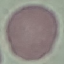 Malaria status: uninfected. Cell patch, automatically extracted from a larger field of view and resized to 64 × 64 pixels. Thin blood smear. Photographed with a smartphone camera at the microscope eyepiece. Giemsa stain.